Classify this cell by malaria status.
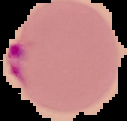
Parasitized.

Summary:
  - Preparation: thin blood smear
  - Image size: 127×121 pixels
  - Image type: cell region segmented out of the field of view; surrounding area masked to black